State which parasite is depicted.
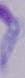
A trypanosome.

Captured at 1000x magnification. Micrograph.